State the preparation type.
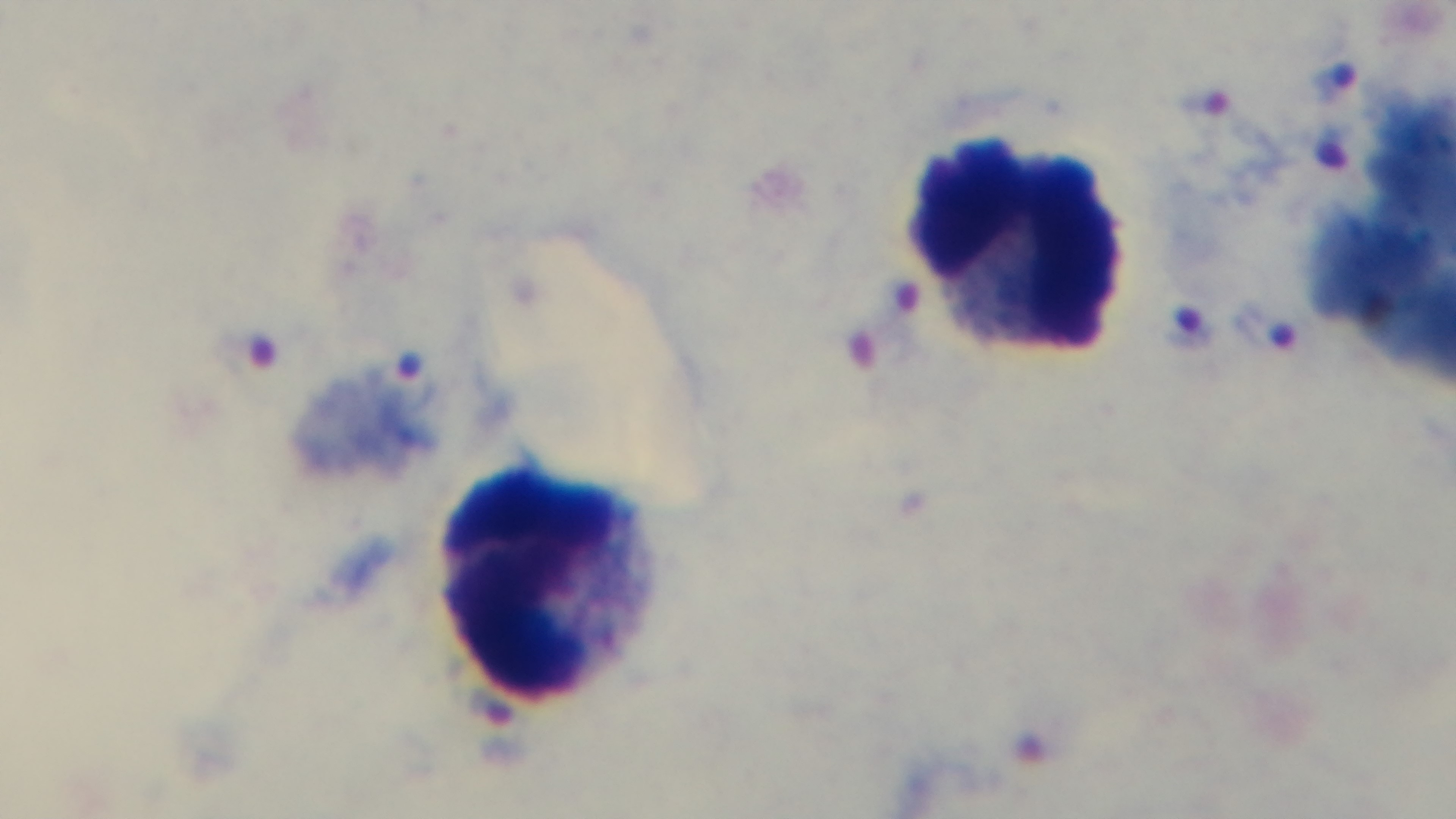
Thick.

{
  "field_of_view": "one from the slide",
  "objective": "100x oil immersion",
  "malaria_status": "infected",
  "stain": "Giemsa",
  "modality": "light microscopy",
  "capture": "mounted 4K digital camera"
}